Assess the morphology of the red blood cells.
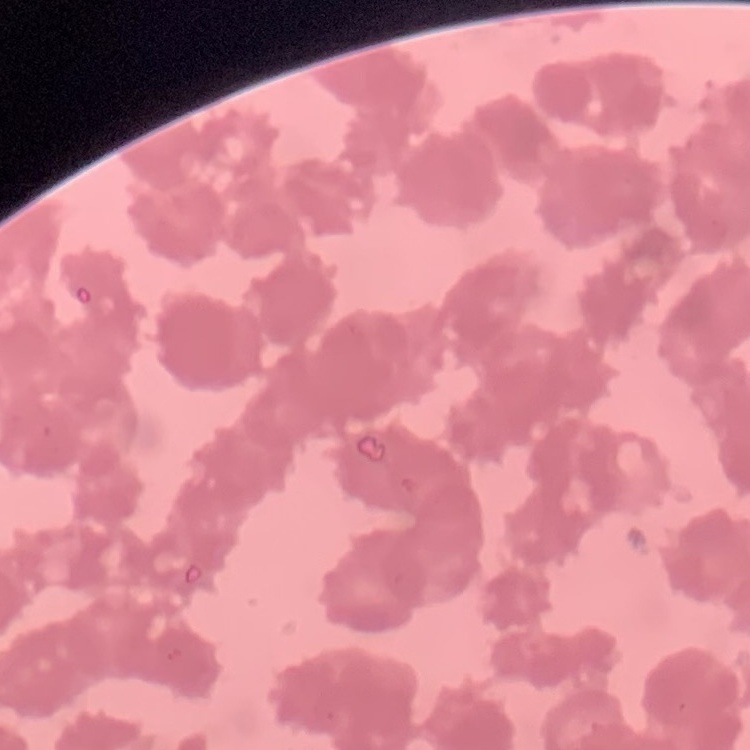

Rouleaux formation.

Field's or Giemsa stain. One tile cut from a larger photomicrograph. Thin peripheral smear.